Assess this cell for malaria.
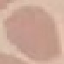
Uninfected.

Thin smear of blood. Photographed with a smartphone camera at the microscope eyepiece. Cell patch, automatically extracted from a larger field of view and resized to 64 × 64 pixels. Giemsa stain.